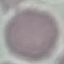
Malaria status: uninfected. Giemsa-stained preparation. Automatically extracted cell patch, resized to 64 × 64 pixels. Thin blood smear. Acquired by smartphone through the microscope eyepiece.